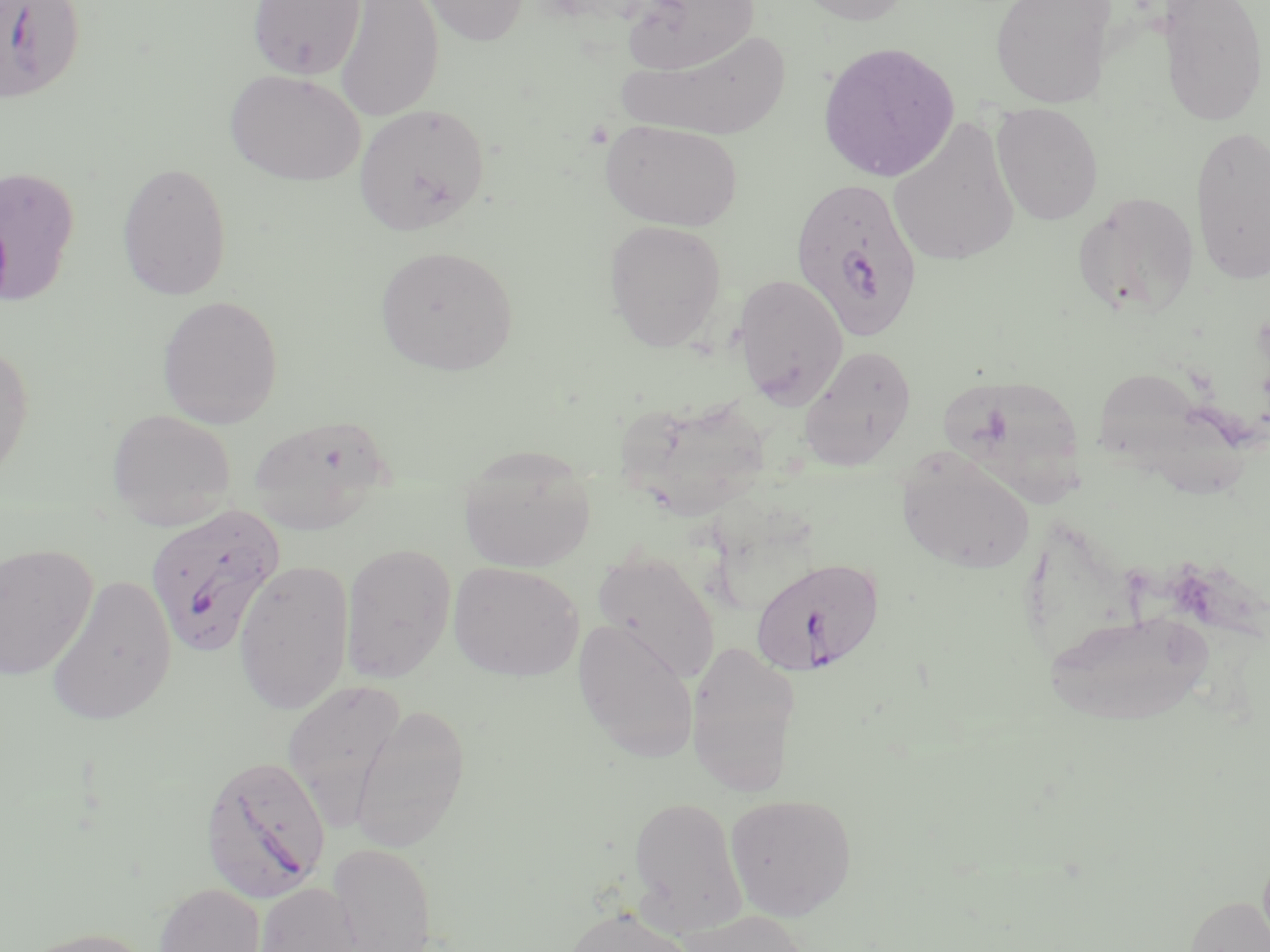
Summary:
  - Coordinate format: approximate bounding boxes as named x1/y1/x2/y2 corners in pixels
  - Uninfected red blood cell locations: (x1=247, y1=0, x2=366, y2=79), (x1=334, y1=0, x2=444, y2=121), (x1=420, y1=0, x2=528, y2=46), (x1=792, y1=0, x2=914, y2=26), (x1=990, y1=0, x2=1116, y2=107), (x1=618, y1=1, x2=762, y2=74), (x1=1158, y1=1, x2=1268, y2=126), (x1=620, y1=29, x2=790, y2=141), (x1=817, y1=41, x2=960, y2=183), (x1=225, y1=69, x2=366, y2=186), (x1=991, y1=102, x2=1104, y2=225), (x1=353, y1=103, x2=490, y2=236), (x1=888, y1=116, x2=1021, y2=266), (x1=600, y1=119, x2=743, y2=231), (x1=1189, y1=123, x2=1270, y2=284), (x1=116, y1=162, x2=233, y2=301), (x1=0, y1=165, x2=80, y2=307), (x1=1073, y1=192, x2=1201, y2=319), (x1=604, y1=219, x2=727, y2=352), (x1=375, y1=244, x2=518, y2=376), (x1=733, y1=274, x2=849, y2=408), (x1=156, y1=294, x2=284, y2=429), (x1=0, y1=339, x2=35, y2=487), (x1=800, y1=345, x2=917, y2=471), (x1=937, y1=373, x2=1087, y2=504), (x1=619, y1=393, x2=774, y2=521), (x1=106, y1=408, x2=236, y2=529), (x1=248, y1=413, x2=393, y2=534), (x1=458, y1=445, x2=598, y2=573), (x1=896, y1=448, x2=1036, y2=575), (x1=341, y1=542, x2=456, y2=683), (x1=0, y1=544, x2=98, y2=680), (x1=591, y1=549, x2=720, y2=684), (x1=234, y1=559, x2=354, y2=716), (x1=448, y1=561, x2=584, y2=681), (x1=45, y1=573, x2=177, y2=726), (x1=1045, y1=609, x2=1213, y2=726), (x1=573, y1=618, x2=701, y2=763), (x1=685, y1=640, x2=801, y2=798), (x1=282, y1=679, x2=406, y2=828), (x1=349, y1=704, x2=470, y2=852), (x1=724, y1=793, x2=857, y2=921), (x1=627, y1=795, x2=747, y2=935), (x1=326, y1=842, x2=438, y2=952), (x1=154, y1=882, x2=266, y2=952), (x1=251, y1=882, x2=364, y2=952), (x1=1184, y1=895, x2=1270, y2=952), (x1=559, y1=906, x2=701, y2=952), (x1=675, y1=909, x2=815, y2=952), (x1=15, y1=926, x2=157, y2=952)
  - Plasmodium falciparum-infected red blood cell locations: (x1=0, y1=1, x2=85, y2=103), (x1=789, y1=177, x2=925, y2=341), (x1=144, y1=503, x2=286, y2=658), (x1=750, y1=555, x2=886, y2=677), (x1=200, y1=753, x2=331, y2=903)
  - Slide-level diagnosis: Plasmodium falciparum
  - Field of view: one of a larger specimen
  - Stain: May-Grünwald-Giemsa
  - Magnification: 1000x
  - Image size: 1270×952 pixels
  - Preparation: thin blood film
  - Modality: light microscopy